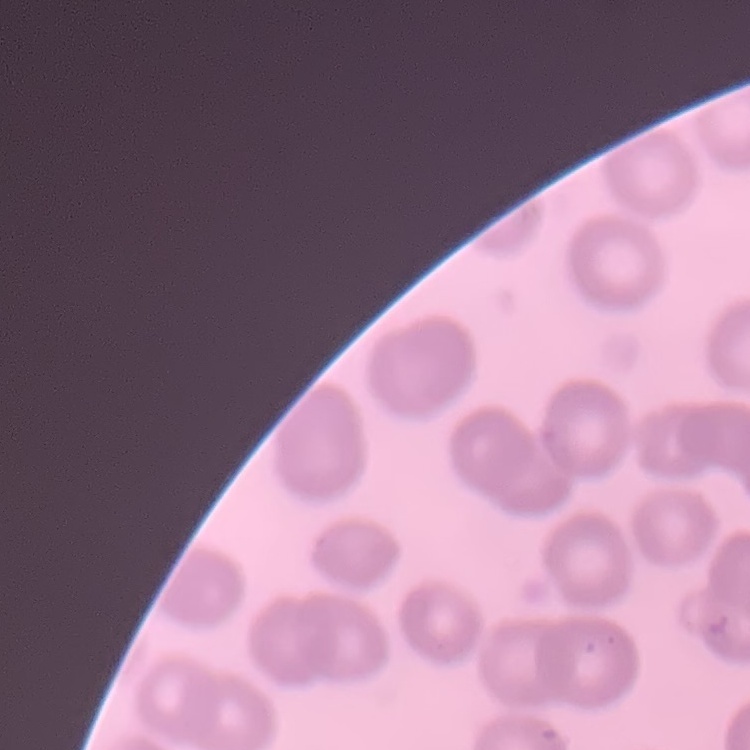 The red blood cells show no rouleaux formation. Thin blood smear. Stained with either Field's or Giemsa. One tile cut from a larger photomicrograph.